Report the malaria status of this cell.
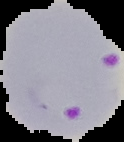
Parasitized.

From a thin blood film. Cell region segmented out of the field of view; the surrounding area is masked to black. Image is 124×142 pixels.